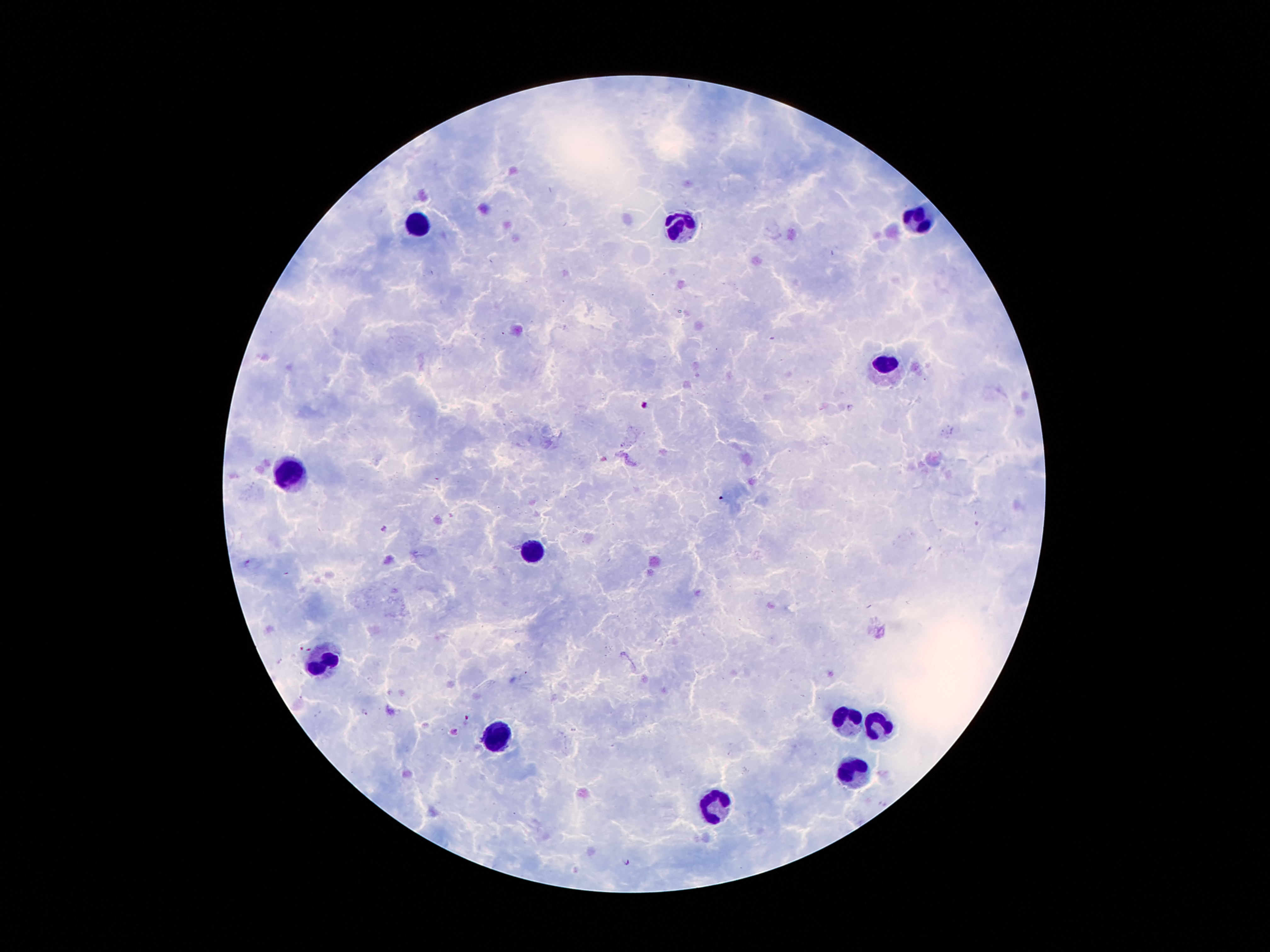
Giemsa-stained preparation. Thick blood film. Single field of view. Image is 1270×952 pixels. 100x magnification. Patient malaria status: infected with Plasmodium falciparum. Smartphone photograph taken through the microscope eyepiece.